Comment on the morphology of the red blood cells.
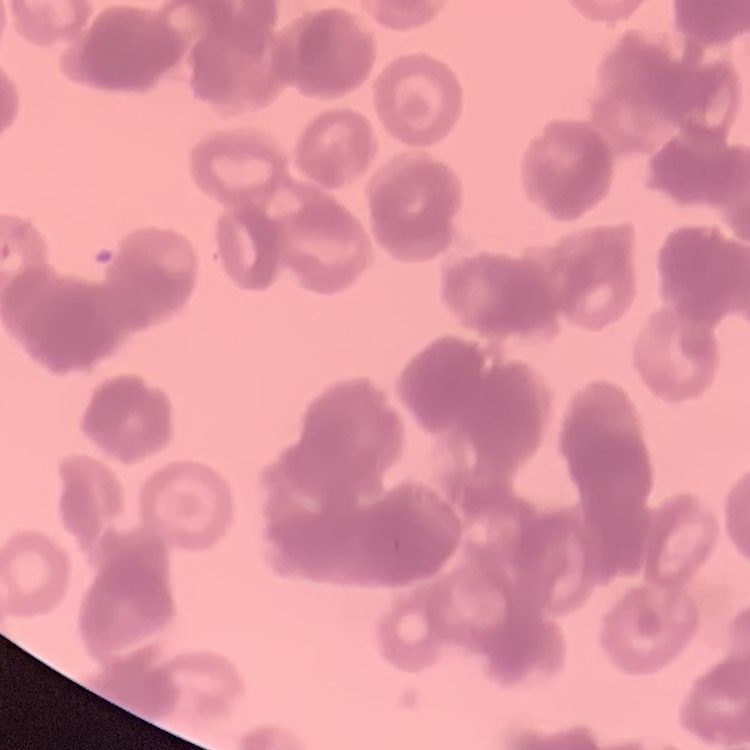

They show rouleaux formation.

Field's or Giemsa stain. Thin blood smear. One tile cut from a larger photomicrograph.